State which parasite is depicted.
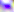
This is Toxoplasma gondii.

Summary:
  - Modality: micrograph
  - Magnification: 400x